Comment on the morphology of the erythrocytes.
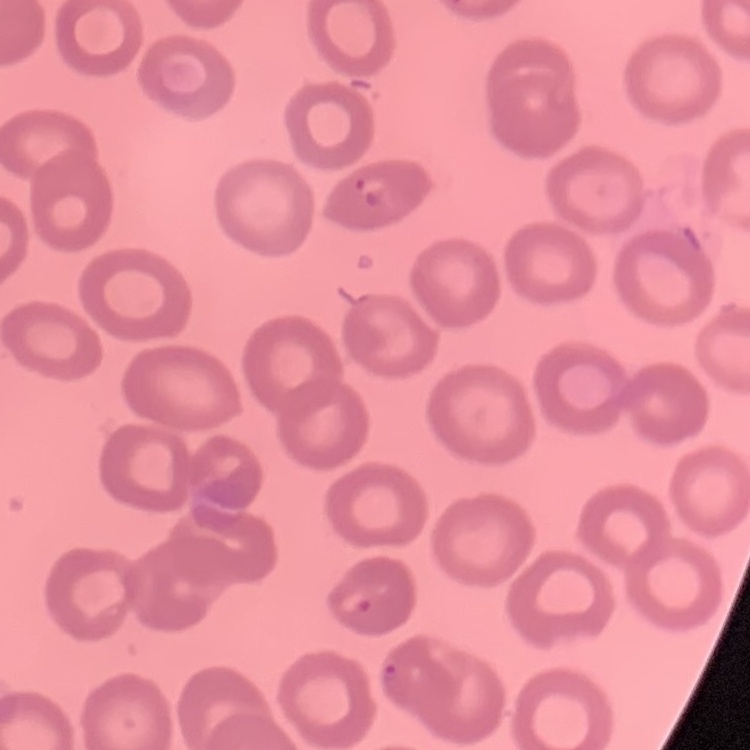

They show no rouleaux formation.

Stained with either Field's or Giemsa. Thin blood smear. Square crop of a larger photomicrograph.